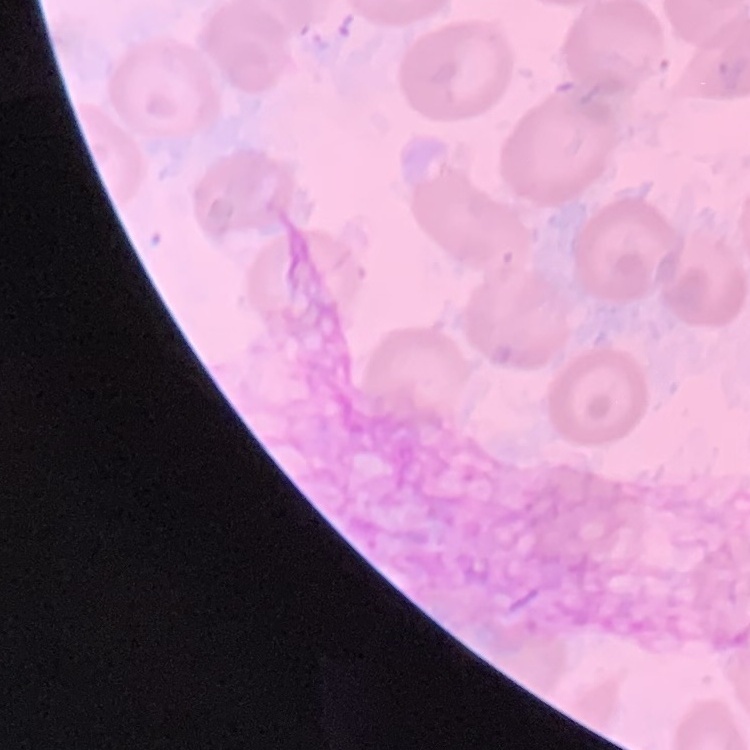
red blood cell morphology = no rouleaux formation
preparation = thin blood film
stain = Field's or Giemsa
image type = square crop of a larger photomicrograph